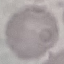 Result: no malaria parasites detected. Giemsa stain. Thin smear of blood. Photographed with a smartphone camera at the microscope eyepiece. Automatically extracted cell patch, resized to 64 × 64 pixels.